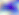

Summary:
  - Modality: micrograph
  - Magnification: 400x
  - Identification: Toxoplasma gondii